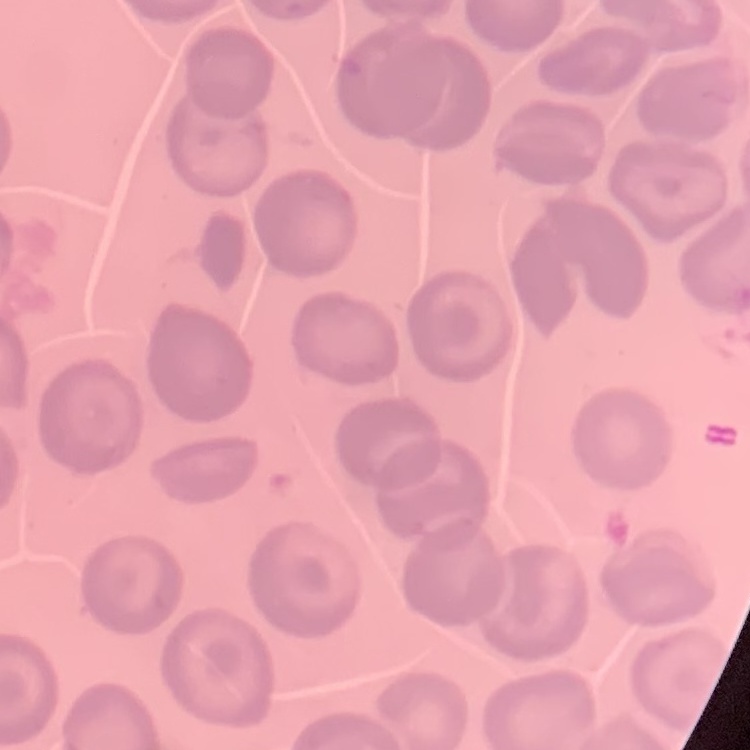 The erythrocytes exhibit no rouleaux formation. One tile cut from a larger photomicrograph. Stained with either Field's or Giemsa. Thin blood smear.